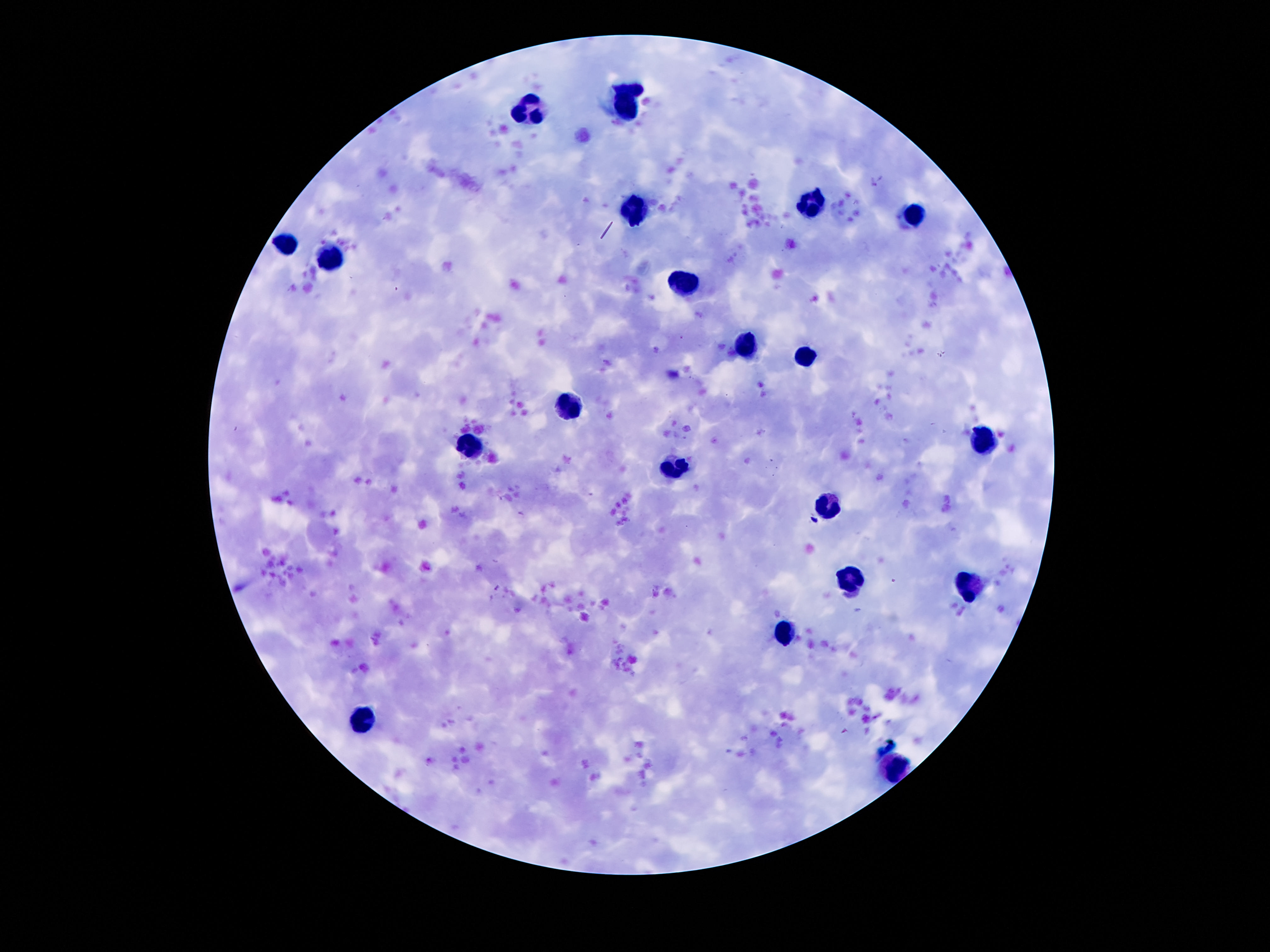
leukocyte locations = approximate object centers, in pixels from the top-left corner: (x=627, y=107), (x=529, y=108), (x=810, y=205), (x=634, y=212), (x=914, y=215), (x=285, y=248), (x=327, y=259), (x=690, y=280), (x=746, y=346), (x=805, y=359), (x=569, y=408), (x=986, y=439), (x=474, y=448), (x=672, y=467), (x=828, y=504), (x=849, y=581), (x=971, y=590), (x=784, y=633), (x=361, y=724), (x=894, y=768)
magnification = 100x
stain = Giemsa
preparation = thick blood film
patient malaria status = negative
capture = smartphone camera through the microscope eyepiece
field of view = single
image size = 1270×952 pixels